Classify this cell by malaria status.
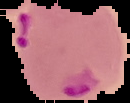

It is parasitized.

image size = 130×103 pixels
image type = cell region segmented out of the field of view; surrounding area masked to black
preparation = thin blood film